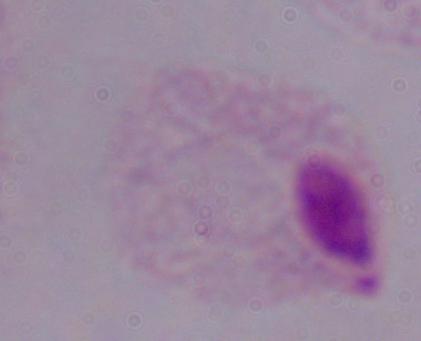
1000x magnification. A trichomonad is seen. Micrograph.